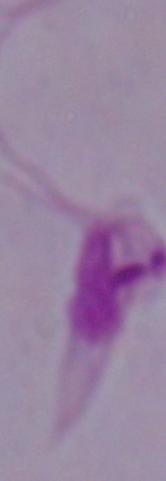
Summary:
  - Modality: micrograph
  - Identification: Leishmania
  - Magnification: 1000x